Report the malaria status of this cell.
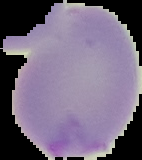
Parasitized.

From a thin blood film. Image is 142×160 pixels. The area outside the segmented cell region is set to black.